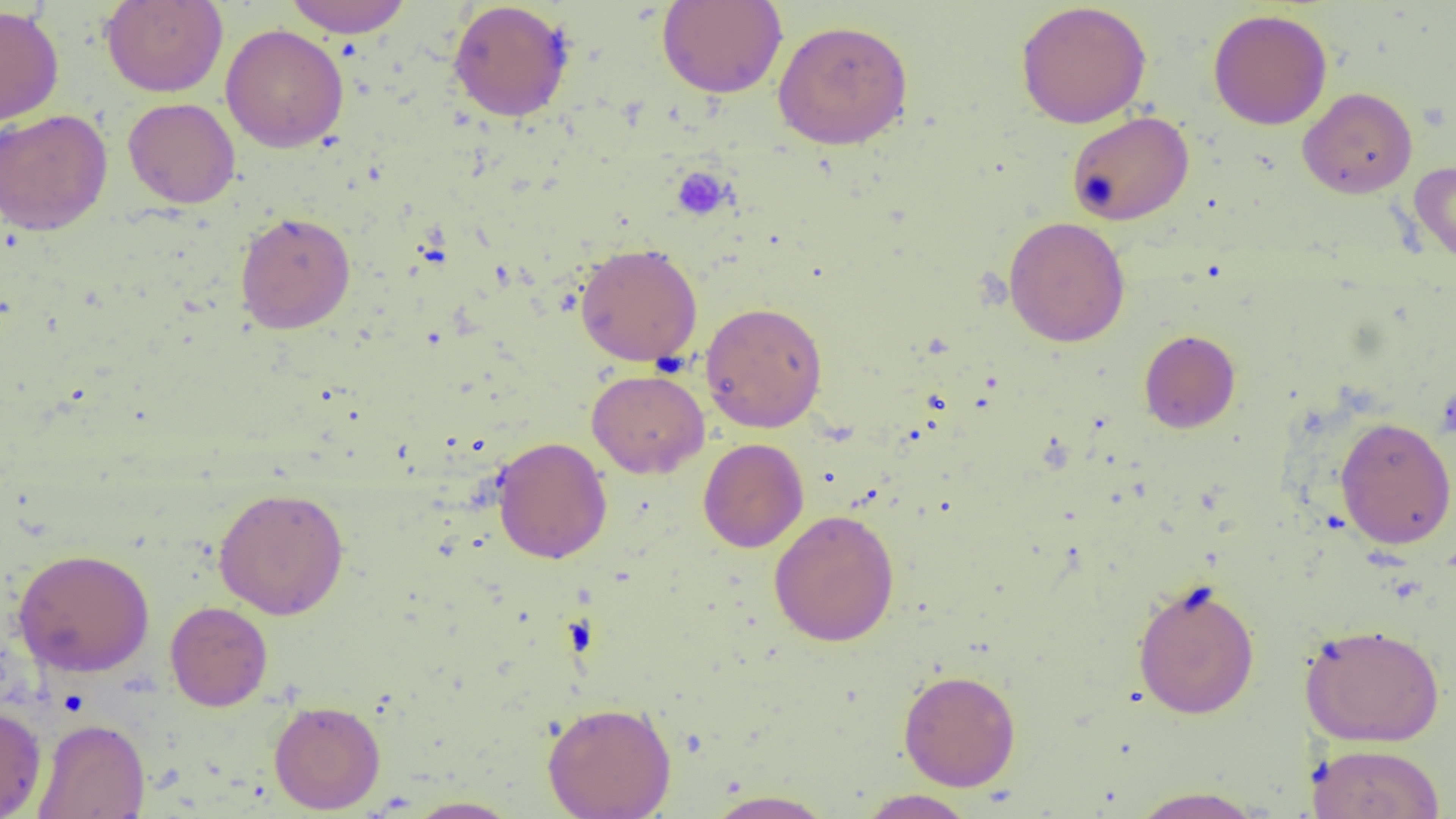

Summary:
  - Coordinate format: approximate bounding boxes as (x1, y1, x2, y2) in pixels
  - Uninfected red blood cell locations: (282, 0, 413, 38), (657, 0, 788, 99), (101, 1, 228, 97), (448, 1, 574, 122), (1015, 1, 1151, 128), (0, 5, 64, 128), (1208, 9, 1332, 130), (772, 19, 913, 149), (221, 24, 349, 152), (1298, 87, 1418, 199), (123, 98, 240, 209), (0, 108, 113, 236), (1067, 111, 1194, 225), (1409, 160, 1456, 267), (234, 212, 356, 333), (1004, 216, 1130, 347), (575, 242, 703, 366), (700, 302, 828, 433), (1139, 329, 1240, 433), (587, 369, 710, 478), (1334, 416, 1456, 549), (492, 437, 612, 564), (698, 438, 809, 553), (213, 487, 350, 620), (769, 509, 900, 646), (12, 547, 155, 677), (1132, 579, 1260, 719), (165, 601, 273, 711), (1300, 623, 1445, 747), (898, 670, 1021, 791), (268, 699, 386, 814), (542, 701, 676, 819), (0, 706, 46, 818), (33, 718, 150, 819), (1307, 743, 1446, 819), (1128, 786, 1269, 818), (703, 789, 836, 818), (857, 789, 976, 818), (402, 796, 522, 818)
  - Platelet locations: (671, 166, 733, 221)
  - Slide-level diagnosis: no evidence of blood parasites
  - Image size: 1456×819 pixels
  - Magnification: 1000x
  - Preparation: thin blood film
  - Modality: optical microscopy
  - Field of view: one of a larger specimen